Assess this cell for malaria.
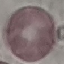
Uninfected.

preparation = thin blood smear
capture = smartphone camera at the microscope eyepiece
stain = Giemsa
image type = automatically extracted cell patch, resized to 64 × 64 pixels